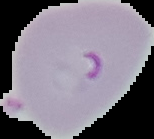 Malaria status: parasitized. Image is 154×139 pixels. Segmented cell region on a black background. From a thin blood film.